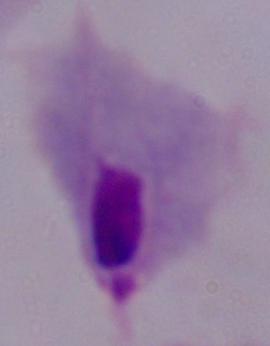 Captured at 1000x magnification. A trichomonad is shown. Photomicrograph.